Point out each leukocyte.
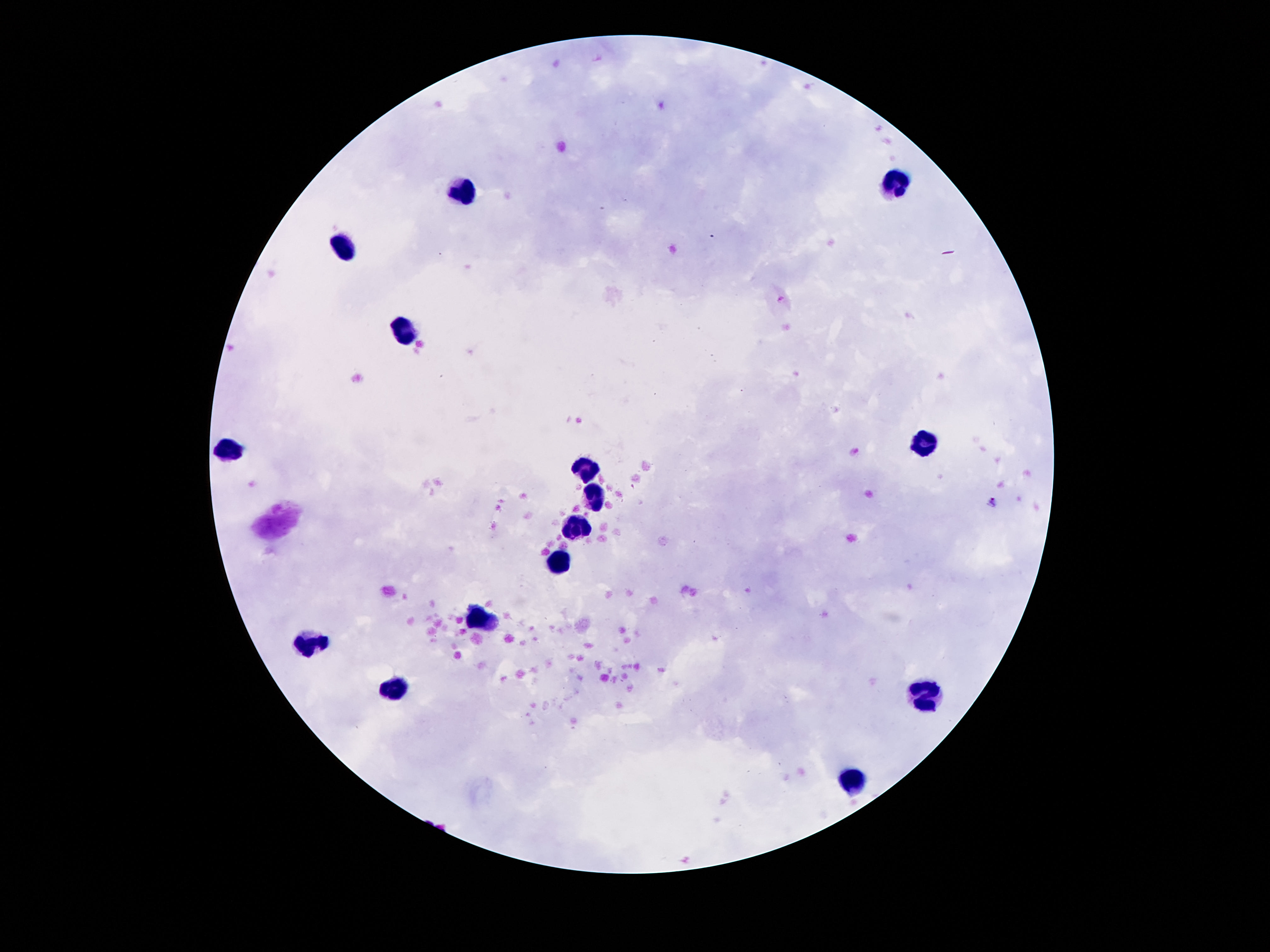
Approximate centers as [x, y] in pixels.
Leukocytes: [894, 186], [458, 193], [346, 249], [406, 327], [923, 445], [230, 448], [582, 471], [595, 498], [577, 525], [558, 564], [479, 616], [311, 642], [395, 690], [923, 693], [857, 779].

image size = 1270×952 pixels
stain = Giemsa
magnification = 100x
preparation = thick blood film
patient malaria status = not infected
field of view = one from this slide
capture = smartphone camera through the microscope eyepiece